State the blood parasite species.
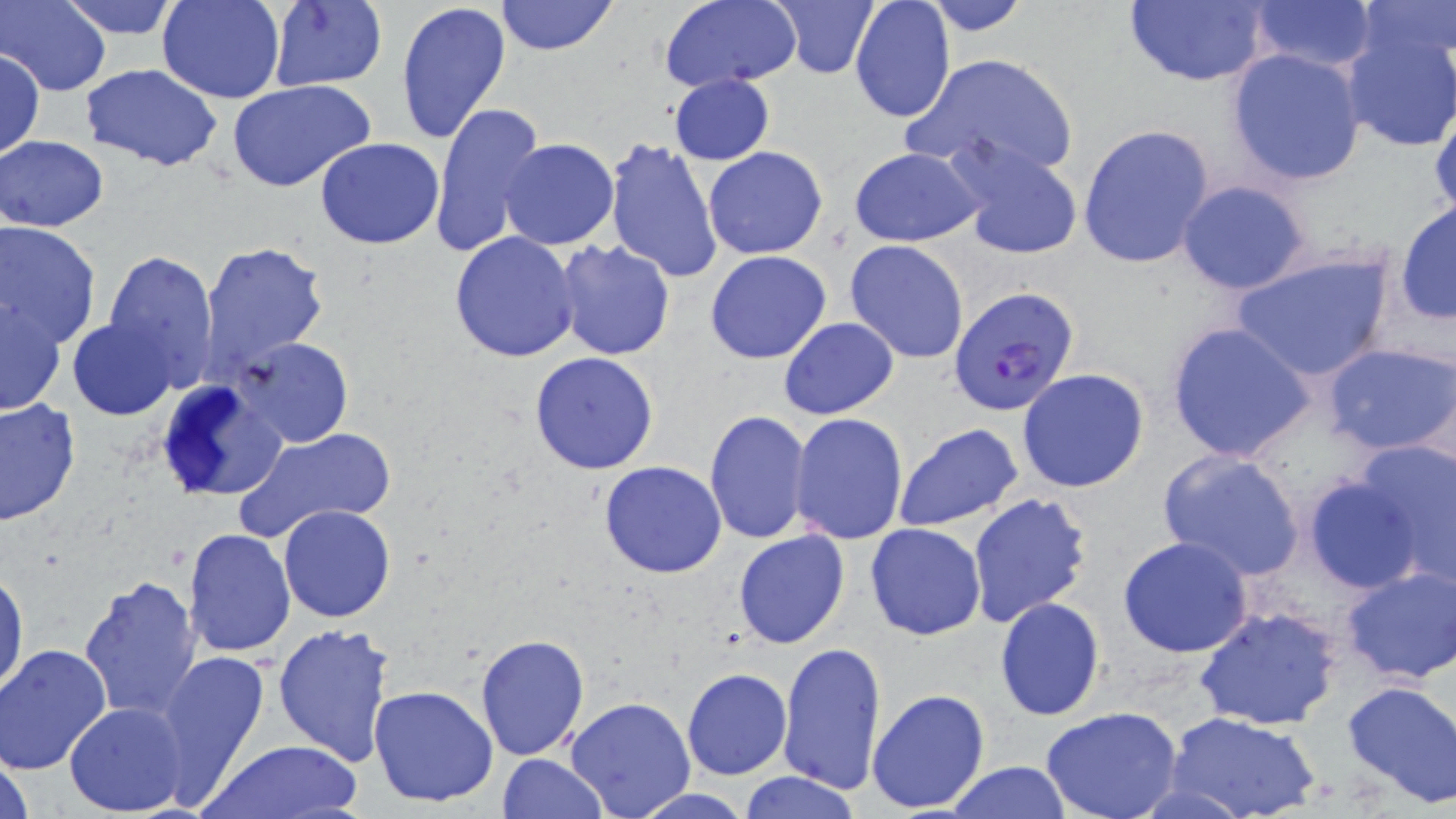
Plasmodium falciparum.

field of view = one of a larger specimen
preparation = thin blood film
image size = 1456×819 pixels
Plasmodium falciparum-infected red blood cell locations = approximate bounding boxes as (x1, y1, x2, y2) in pixels: (948, 284, 1079, 418)
modality = optical microscopy
stain = May-Grünwald-Giemsa
uninfected red blood cell locations = approximate bounding boxes as (x1, y1, x2, y2) in pixels: (2, 0, 109, 96), (55, 0, 183, 39), (158, 0, 285, 104), (496, 0, 616, 56), (658, 0, 804, 90), (849, 0, 956, 121), (919, 0, 1034, 35), (1121, 0, 1268, 87), (1242, 0, 1380, 76), (394, 1, 511, 148), (770, 1, 880, 79), (262, 2, 388, 92), (1353, 2, 1456, 61), (1339, 26, 1456, 152), (0, 49, 43, 158), (1227, 49, 1368, 186), (906, 52, 1081, 181), (81, 64, 225, 169), (668, 73, 775, 164), (227, 79, 374, 192), (1429, 95, 1456, 224), (427, 102, 547, 261), (1078, 123, 1216, 270), (943, 134, 1086, 262), (1, 135, 108, 231), (316, 137, 445, 249), (499, 138, 619, 251), (604, 138, 725, 283), (848, 146, 986, 247), (703, 147, 829, 260), (1175, 180, 1316, 296), (1394, 201, 1456, 324), (0, 221, 102, 347), (448, 231, 581, 362), (553, 238, 676, 360), (843, 240, 968, 364), (201, 241, 330, 373), (103, 249, 220, 385), (1231, 249, 1395, 383), (705, 250, 832, 364), (1, 293, 67, 418), (778, 317, 900, 420), (68, 318, 178, 419), (1166, 321, 1316, 464), (235, 336, 353, 449), (1322, 341, 1456, 455), (529, 351, 660, 476), (1017, 369, 1150, 493), (152, 375, 288, 505), (1, 396, 80, 527), (704, 410, 810, 544), (789, 412, 908, 544), (892, 423, 1024, 532), (234, 425, 399, 544), (1351, 438, 1456, 586), (1154, 447, 1306, 581), (599, 461, 727, 579), (1303, 476, 1426, 593), (967, 492, 1093, 626), (278, 504, 396, 622), (865, 523, 985, 640), (184, 528, 295, 657), (733, 529, 851, 650), (1117, 535, 1255, 658), (1339, 566, 1456, 685), (0, 567, 27, 699), (79, 573, 204, 723), (994, 597, 1104, 721), (1191, 605, 1343, 733), (273, 622, 398, 767), (475, 634, 589, 760), (778, 641, 887, 796), (1, 643, 112, 775), (154, 648, 270, 801), (681, 668, 792, 780), (1342, 678, 1456, 808), (368, 685, 498, 807), (866, 687, 991, 813), (564, 696, 696, 819), (65, 702, 189, 816), (1041, 708, 1184, 819), (1168, 712, 1320, 819), (199, 739, 361, 819), (1, 748, 34, 819), (499, 754, 607, 817), (943, 762, 1074, 818), (738, 772, 863, 818), (630, 788, 755, 818)
magnification = 1000x